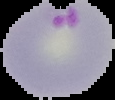

Summary:
  - Malaria status: parasitized
  - Image type: segmented cell region with the area outside set to black
  - Image size: 115×100 pixels
  - Preparation: thin blood film